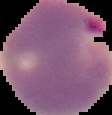

Summary:
  - Image type: segmented cell region with the area outside set to black
  - Image size: 112×115 pixels
  - Preparation: thin blood smear
  - Malaria status: parasitized